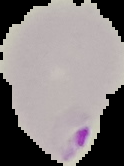
Summary:
  - Preparation: thin blood film
  - Image type: segmented cell region with the area outside set to black
  - Result: Plasmodium parasites identified
  - Image size: 124×166 pixels